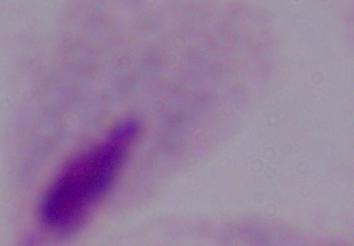
Summary:
  - Modality: photomicrograph
  - Magnification: 1000x
  - Identification: trichomonad